Identify the preparation type.
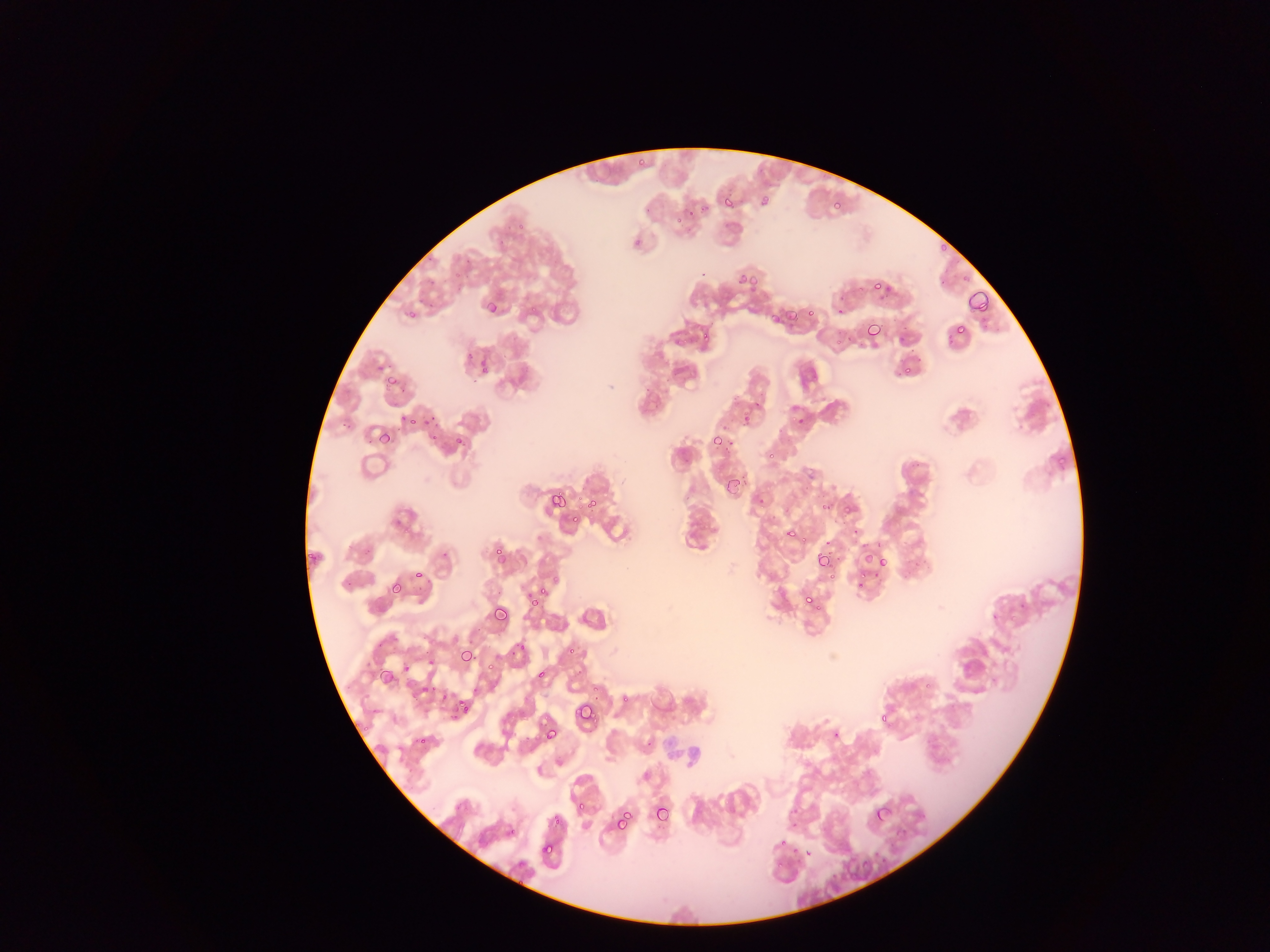

This is a thin smear.

Approximate bounding boxes as left top right bottom in pixels. Plasmodium parasite locations: 636 156 648 171; 724 196 735 209; 761 198 774 211; 830 199 846 213; 699 204 711 214; 686 206 696 216; 676 217 688 226; 939 239 950 255; 737 271 745 282; 747 273 759 286; 873 278 881 290; 966 290 990 311; 485 301 502 314; 780 302 797 320; 806 308 816 321; 409 310 419 322; 767 311 783 324; 863 322 881 339; 955 325 966 334; 702 330 714 343; 477 362 493 376; 902 366 910 374; 386 375 403 388; 429 409 438 422; 789 411 797 421; 397 414 408 421; 408 418 419 428; 379 428 393 446; 430 435 440 442; 456 435 464 448; 708 437 721 448; 766 453 773 462; 1056 456 1070 465; 724 476 742 494; 548 492 567 517; 576 492 587 512; 587 494 601 513; 757 499 768 508; 821 502 828 510; 842 506 854 515; 571 513 580 524; 785 525 799 540; 799 536 808 542; 823 541 834 546; 495 546 510 562; 810 547 832 569; 307 551 317 561; 862 551 876 567; 878 557 887 569; 414 569 424 580; 872 571 881 576; 857 572 865 578; 553 573 560 583; 828 573 838 581; 856 579 867 592; 389 581 406 595; 539 583 547 595; 806 586 817 608; 529 596 540 611; 815 602 822 613; 494 606 508 622; 568 645 577 655; 459 648 474 664; 487 661 495 672; 537 664 547 678; 925 681 931 690; 430 684 439 696; 590 684 601 694; 454 693 463 705; 621 695 629 703; 577 703 593 719; 461 704 471 715; 876 714 891 722; 362 728 371 733; 545 730 556 743; 833 733 841 738; 419 738 426 746; 577 798 586 812; 653 803 672 820; 875 805 891 828; 619 810 637 827; 552 816 561 824; 614 819 627 831; 509 829 517 834; 780 840 787 848; 543 845 554 856; 793 847 798 855; 775 861 785 867; 516 877 522 885. Sample from Ghana. Single field of view. Image is 1270×952 pixels. Photographed through a microscope with a mobile-phone camera.